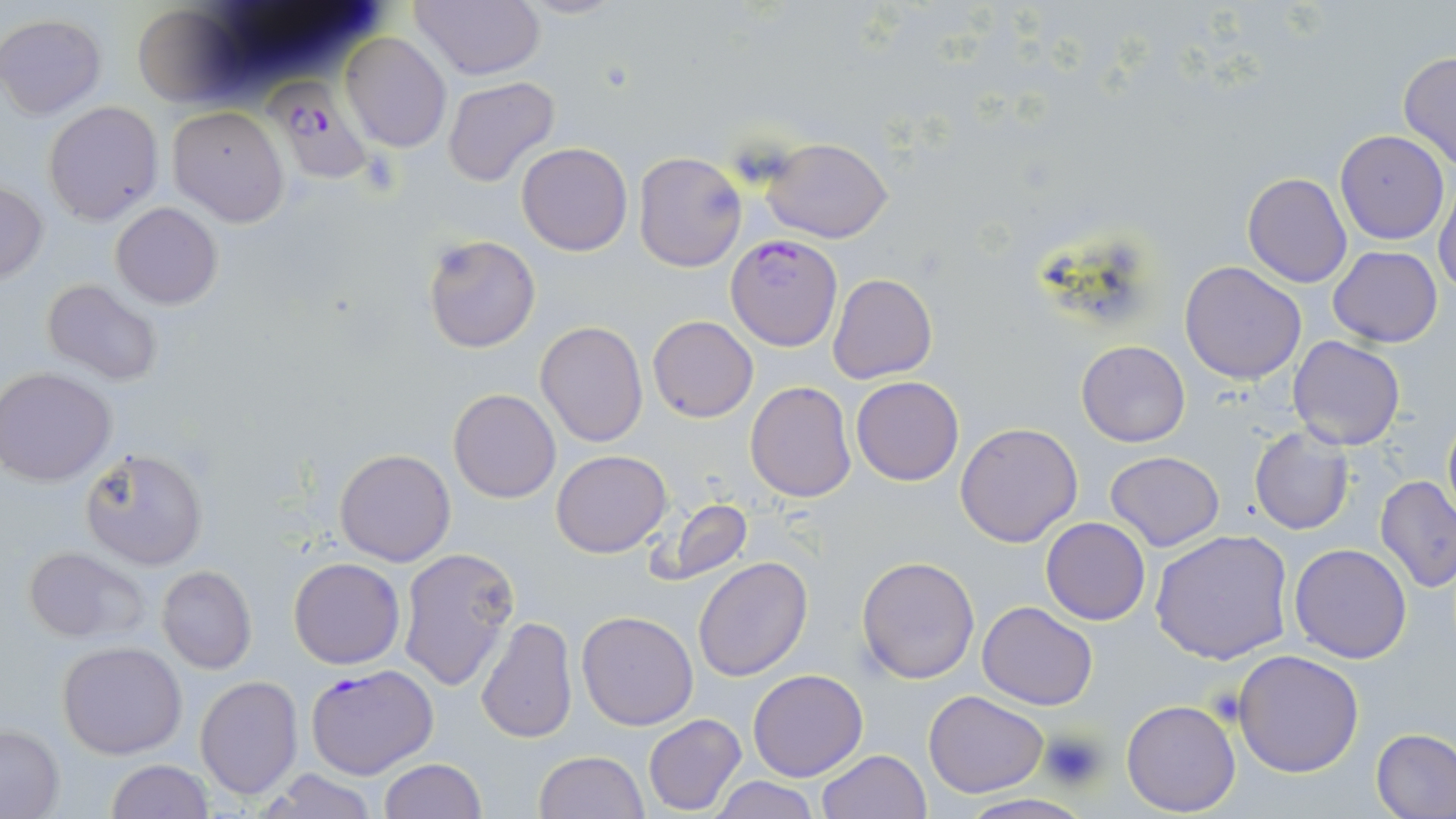
slide-level diagnosis = Plasmodium falciparum
platelet locations = approximate bounding boxes as named x1/y1/x2/y2 corners in pixels: (x1=1040, y1=728, x2=1106, y2=790)
modality = light microscopy
image size = 1456×819 pixels
uninfected red blood cell locations = approximate bounding boxes as named x1/y1/x2/y2 corners in pixels: (x1=411, y1=0, x2=547, y2=80), (x1=130, y1=4, x2=245, y2=107), (x1=0, y1=13, x2=106, y2=119), (x1=341, y1=33, x2=452, y2=152), (x1=1398, y1=50, x2=1456, y2=170), (x1=442, y1=76, x2=560, y2=185), (x1=43, y1=100, x2=164, y2=226), (x1=166, y1=105, x2=290, y2=227), (x1=1335, y1=130, x2=1450, y2=244), (x1=762, y1=136, x2=893, y2=242), (x1=516, y1=141, x2=633, y2=256), (x1=634, y1=152, x2=747, y2=272), (x1=1242, y1=172, x2=1352, y2=290), (x1=0, y1=182, x2=49, y2=284), (x1=1434, y1=184, x2=1456, y2=299), (x1=110, y1=202, x2=223, y2=309), (x1=423, y1=236, x2=540, y2=353), (x1=1329, y1=246, x2=1443, y2=347), (x1=1179, y1=263, x2=1306, y2=385), (x1=828, y1=273, x2=937, y2=384), (x1=41, y1=279, x2=162, y2=385), (x1=648, y1=316, x2=758, y2=422), (x1=535, y1=321, x2=648, y2=447), (x1=1287, y1=336, x2=1405, y2=451), (x1=1076, y1=340, x2=1189, y2=447), (x1=0, y1=367, x2=117, y2=486), (x1=851, y1=376, x2=964, y2=486), (x1=745, y1=380, x2=856, y2=502), (x1=448, y1=388, x2=561, y2=503), (x1=1442, y1=406, x2=1456, y2=526), (x1=954, y1=421, x2=1084, y2=548), (x1=1248, y1=428, x2=1353, y2=535), (x1=78, y1=446, x2=208, y2=570), (x1=334, y1=448, x2=456, y2=567), (x1=552, y1=450, x2=671, y2=556), (x1=1105, y1=450, x2=1225, y2=550), (x1=1377, y1=474, x2=1456, y2=591), (x1=661, y1=499, x2=751, y2=582), (x1=1041, y1=516, x2=1150, y2=624), (x1=1151, y1=529, x2=1294, y2=665), (x1=1288, y1=543, x2=1413, y2=663), (x1=20, y1=545, x2=150, y2=643), (x1=398, y1=547, x2=518, y2=690), (x1=855, y1=555, x2=980, y2=683), (x1=692, y1=556, x2=813, y2=681), (x1=289, y1=557, x2=404, y2=670), (x1=155, y1=565, x2=257, y2=675), (x1=977, y1=602, x2=1099, y2=710), (x1=576, y1=609, x2=700, y2=730), (x1=475, y1=616, x2=578, y2=744), (x1=57, y1=641, x2=187, y2=759), (x1=1233, y1=649, x2=1366, y2=776), (x1=748, y1=669, x2=868, y2=781), (x1=193, y1=676, x2=304, y2=801), (x1=923, y1=689, x2=1050, y2=798), (x1=1121, y1=699, x2=1241, y2=817), (x1=643, y1=713, x2=747, y2=815), (x1=0, y1=724, x2=65, y2=817), (x1=1370, y1=728, x2=1456, y2=819), (x1=814, y1=749, x2=931, y2=819), (x1=533, y1=750, x2=649, y2=819), (x1=379, y1=758, x2=486, y2=818), (x1=106, y1=760, x2=213, y2=818), (x1=257, y1=767, x2=377, y2=819), (x1=710, y1=777, x2=820, y2=818), (x1=957, y1=794, x2=1094, y2=818)
Plasmodium falciparum-infected red blood cell locations = approximate bounding boxes as named x1/y1/x2/y2 corners in pixels: (x1=265, y1=78, x2=381, y2=188), (x1=726, y1=234, x2=842, y2=351), (x1=306, y1=665, x2=439, y2=781)
stain = May-Grünwald-Giemsa
preparation = thin blood film
magnification = 1000x
field of view = one of a larger specimen